Name the parasite shown.
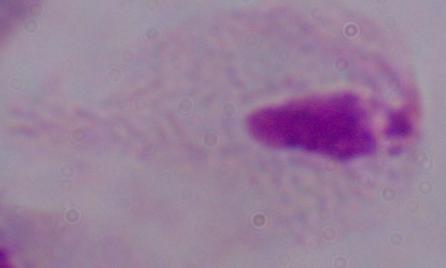
A trichomonad.

Summary:
  - Modality: micrograph
  - Magnification: 1000x